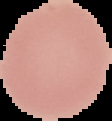

Summary:
  - Image type: segmented cell region with the area outside set to black
  - Image size: 112×121 pixels
  - Preparation: thin blood smear
  - Result: no Plasmodium parasites seen